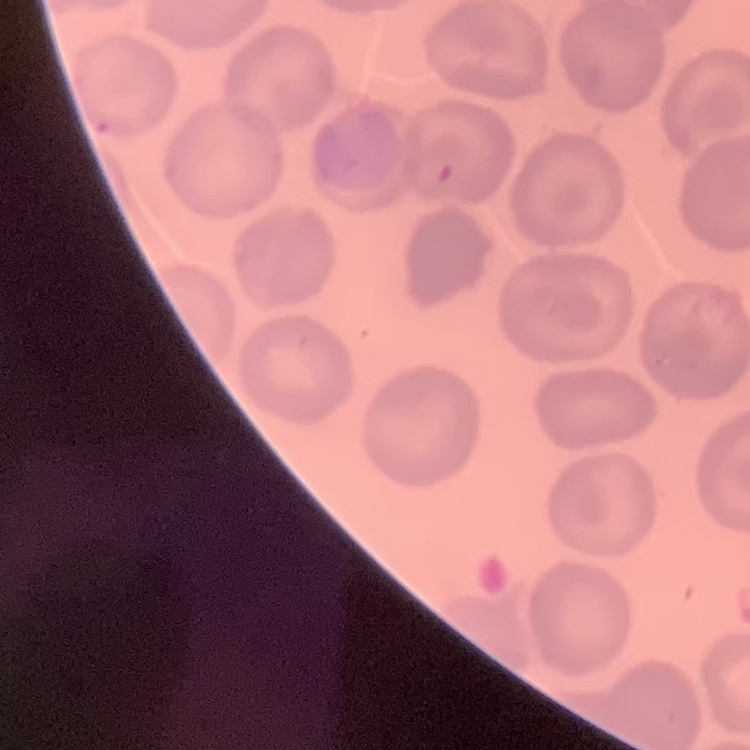

Summary:
  - Red blood cell morphology: no rouleaux formation
  - Preparation: thin blood film
  - Stain: Field's or Giemsa
  - Image type: square crop of a larger photomicrograph